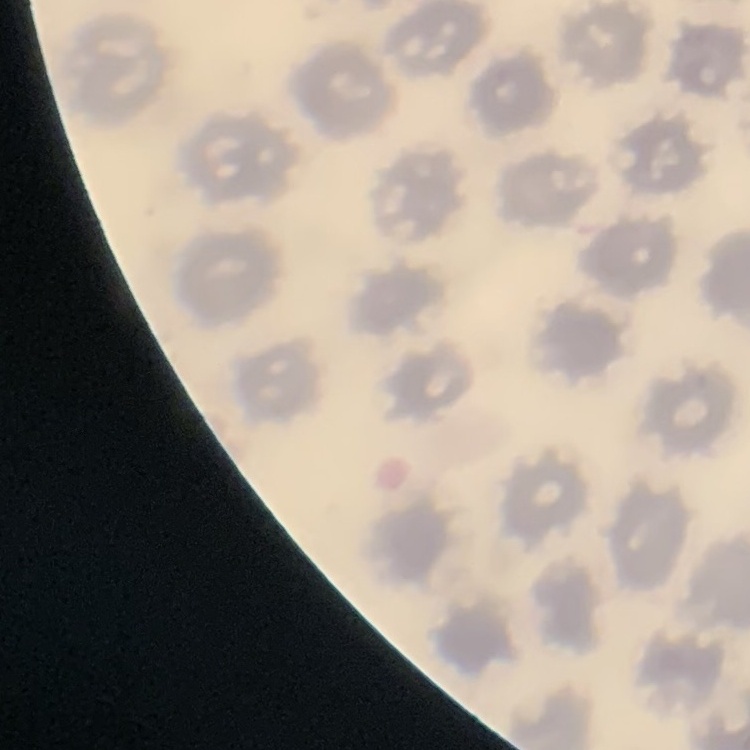

red blood cell morphology = no rouleaux formation
image type = one tile cut from a larger photomicrograph
preparation = thin peripheral smear
stain = Field's or Giemsa